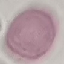

Summary:
  - Result: no malaria parasites seen
  - Preparation: thin blood film
  - Image type: automatically extracted cell patch, resized to 64 × 64 pixels
  - Capture: smartphone through the microscope eyepiece
  - Stain: Giemsa